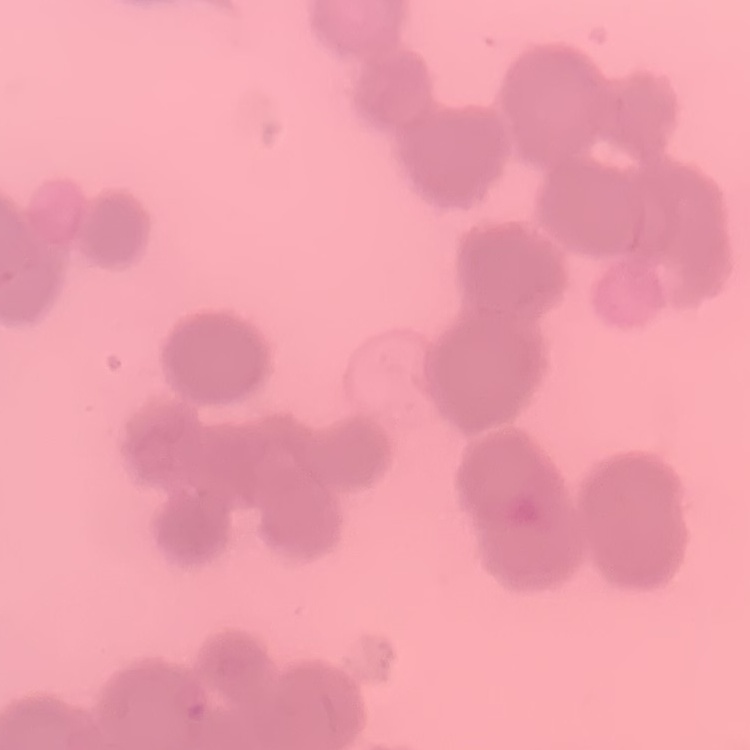

{
  "erythrocyte_morphology": "rouleaux formation",
  "stain": "Field's or Giemsa",
  "preparation": "thin blood film",
  "image_type": "square crop of a larger photomicrograph"
}